State which parasite is depicted.
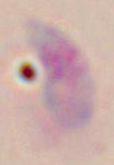
This is Toxoplasma gondii.

modality = photomicrograph
magnification = 1000x